Give the position of every Plasmodium parasite.
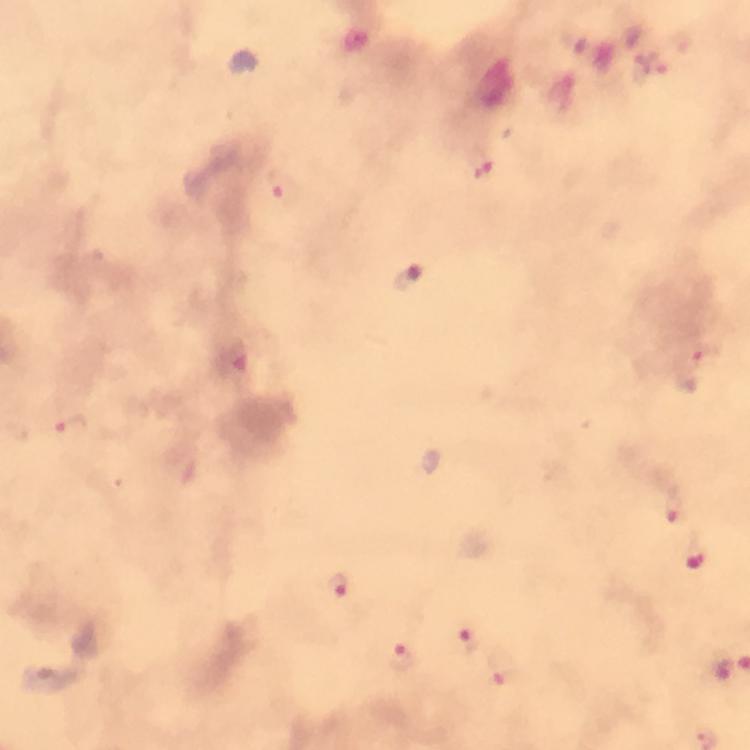
Approximate centers as (x, y) in pixels.
Plasmodium parasites: (483, 173), (282, 187), (409, 278), (707, 352), (233, 361), (71, 425), (676, 505), (695, 557), (337, 587), (468, 641), (402, 658), (719, 668), (502, 672).

image size = 750×750 pixels
preparation = thick blood smear
capture = smartphone mounted on the microscope
immersion oil = used
stain = Giemsa
cropped from = one field of view
magnification = 100x
context = from a diagnostic examination for malaria